Classify this cell by malaria status.
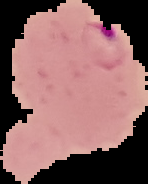

Parasitized.

Summary:
  - Image type: segmented cell region on a black background
  - Image size: 148×184 pixels
  - Preparation: thin blood smear